Give the position of every Plasmodium parasite visible.
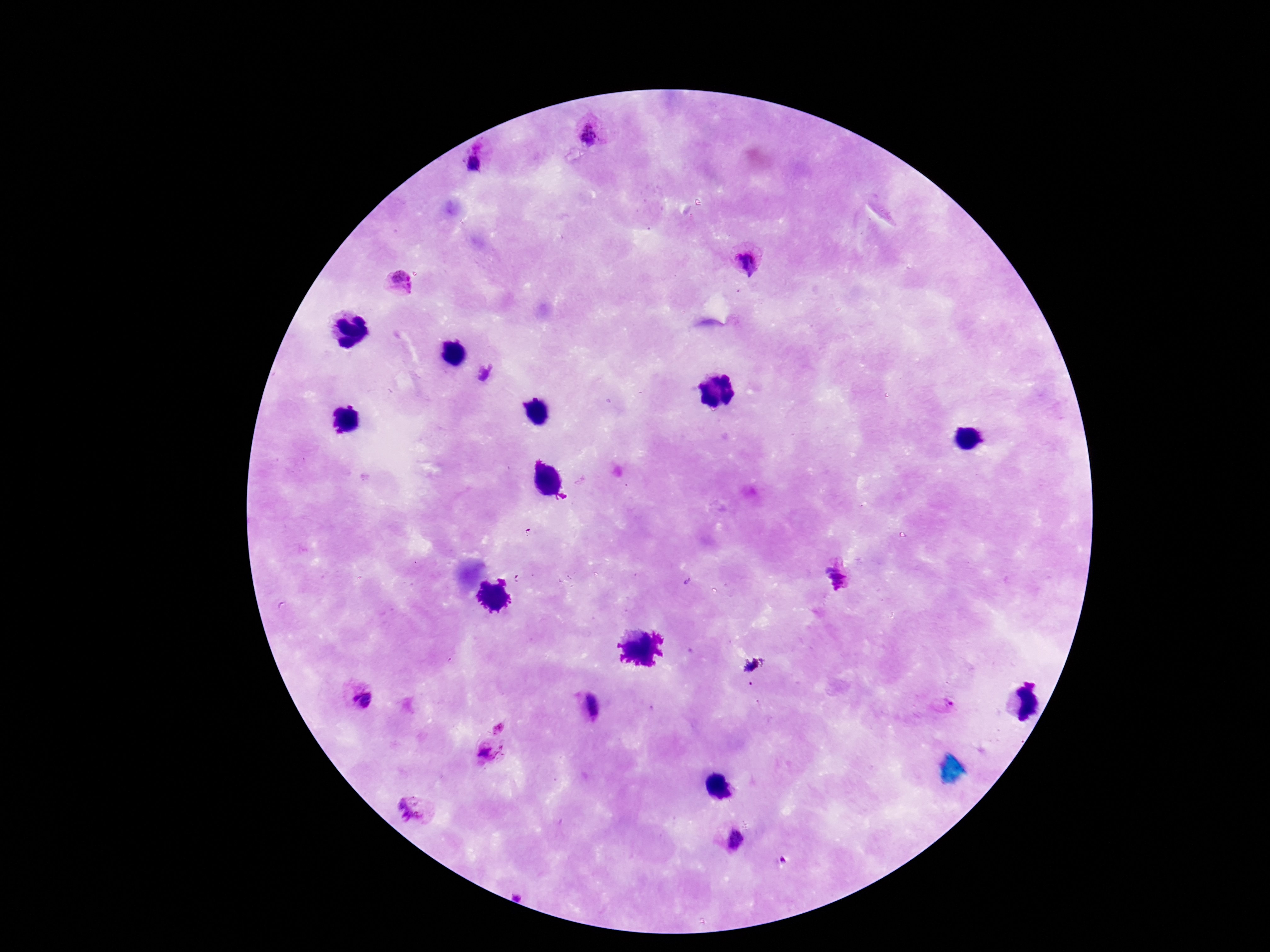

Approximate object centers, in pixels from the top-left corner.
Plasmodium parasites: (x=589, y=133), (x=471, y=163), (x=745, y=264), (x=400, y=282), (x=485, y=374), (x=837, y=575), (x=363, y=700), (x=588, y=706), (x=946, y=706), (x=499, y=726), (x=488, y=752), (x=415, y=806), (x=735, y=842).

Summary:
  - Image size: 1270×952 pixels
  - Magnification: 100x
  - Preparation: thick blood smear
  - Capture: smartphone camera through the microscope eyepiece
  - Patient malaria status: infected
  - Stain: Giemsa
  - Field of view: one from this slide